Describe the morphology of the erythrocytes.
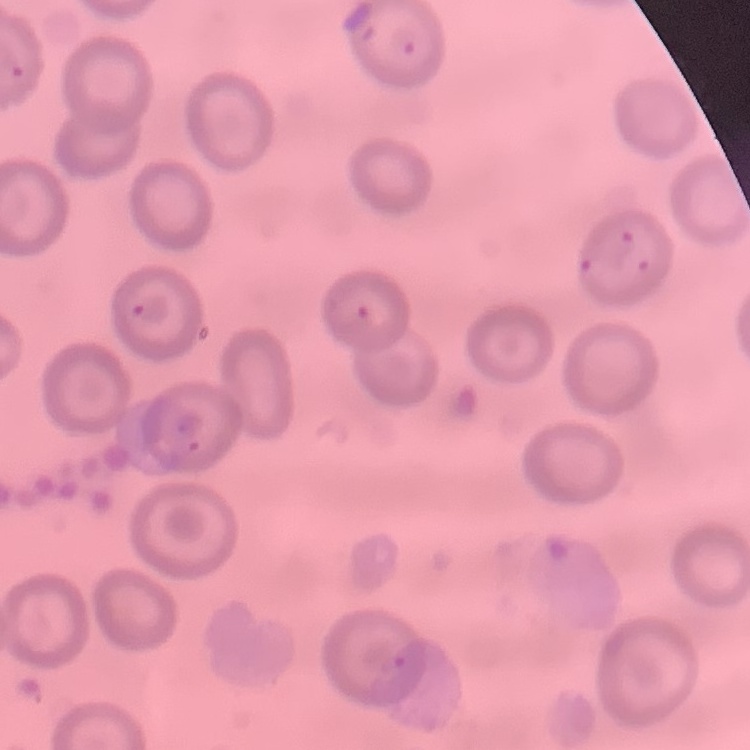
They show no rouleaux formation.

Thin blood smear. One tile cut from a larger photomicrograph. Stained with either Field's or Giemsa.